Classify this cell by malaria status.
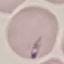
It is parasitized.

Thin smear of blood. Automatically extracted cell patch, resized to 64 × 64 pixels. Photographed with a smartphone camera at the microscope eyepiece. Giemsa stain.